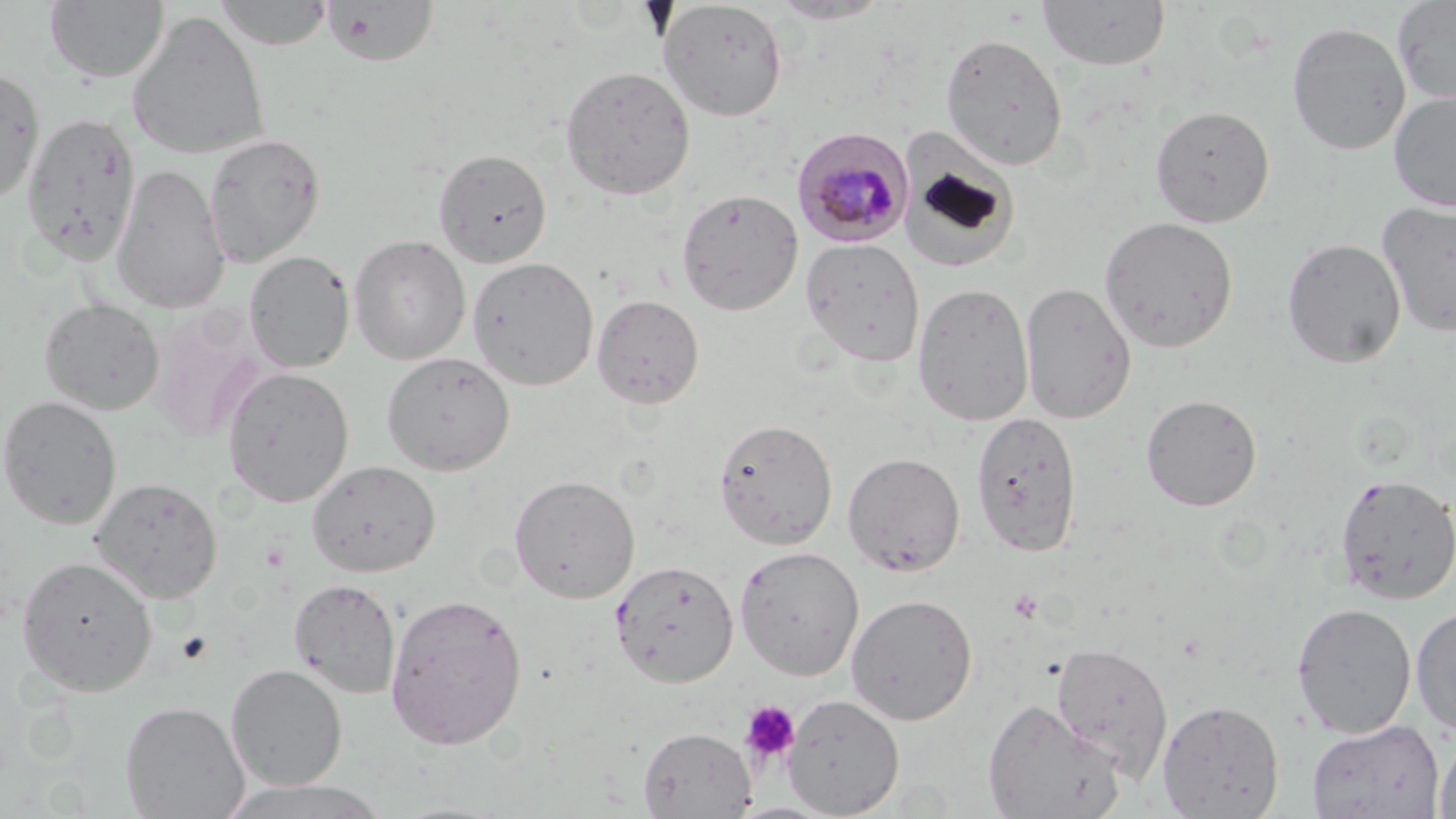

plasmodium_malariae_infected_red_blood_cell_locations: 'approximate bounding boxes as (x1, y1, x2, y2) in pixels: (792, 127, 914, 248)'
slide_level_diagnosis: Plasmodium malariae
preparation: thin blood film
stain: May-Grünwald-Giemsa
uninfected_red_blood_cell_locations: 'approximate bounding boxes as (x1, y1, x2, y2) in pixels: (214, 0, 334, 50), (1037, 0, 1170, 71), (1392, 0, 1456, 105), (45, 1, 169, 82), (324, 1, 440, 68), (658, 1, 788, 121), (768, 1, 890, 24), (127, 10, 270, 160), (1286, 21, 1412, 155), (940, 32, 1069, 171), (560, 65, 696, 200), (0, 67, 45, 206), (1388, 89, 1456, 212), (1149, 104, 1275, 228), (22, 111, 140, 266), (203, 132, 326, 267), (900, 141, 1020, 273), (433, 148, 551, 268), (111, 164, 231, 314), (675, 188, 804, 315), (1377, 201, 1456, 337), (1099, 215, 1239, 354), (349, 234, 471, 364), (1281, 237, 1406, 368), (801, 238, 925, 366), (244, 251, 354, 374), (467, 256, 599, 390), (912, 281, 1034, 426), (1020, 281, 1136, 424), (591, 294, 704, 409), (39, 297, 165, 415), (146, 303, 271, 442), (381, 351, 515, 475), (221, 366, 355, 507), (1141, 393, 1263, 511), (0, 395, 122, 530), (971, 410, 1083, 556), (714, 418, 838, 550), (843, 451, 965, 577), (307, 460, 440, 577), (1334, 472, 1456, 605), (509, 474, 640, 603), (91, 476, 223, 603), (734, 545, 865, 680), (16, 554, 158, 695), (610, 559, 739, 687), (289, 579, 401, 699), (384, 592, 528, 750), (846, 593, 978, 725), (1291, 601, 1417, 738), (1411, 604, 1456, 736), (1051, 641, 1173, 779), (226, 664, 347, 790), (784, 694, 905, 818), (982, 698, 1125, 818), (1157, 698, 1285, 818), (120, 700, 249, 818), (1307, 719, 1444, 819), (637, 726, 756, 818), (1433, 735, 1456, 819), (220, 778, 388, 819)'
modality: optical microscopy
image_size: 1456×819 pixels
field_of_view: one of a larger specimen
platelet_locations: 'approximate bounding boxes as (x1, y1, x2, y2) in pixels: (175, 630, 213, 665), (740, 700, 800, 765)'
magnification: 1000x